Locate every Plasmodium ovale-infected red blood cell.
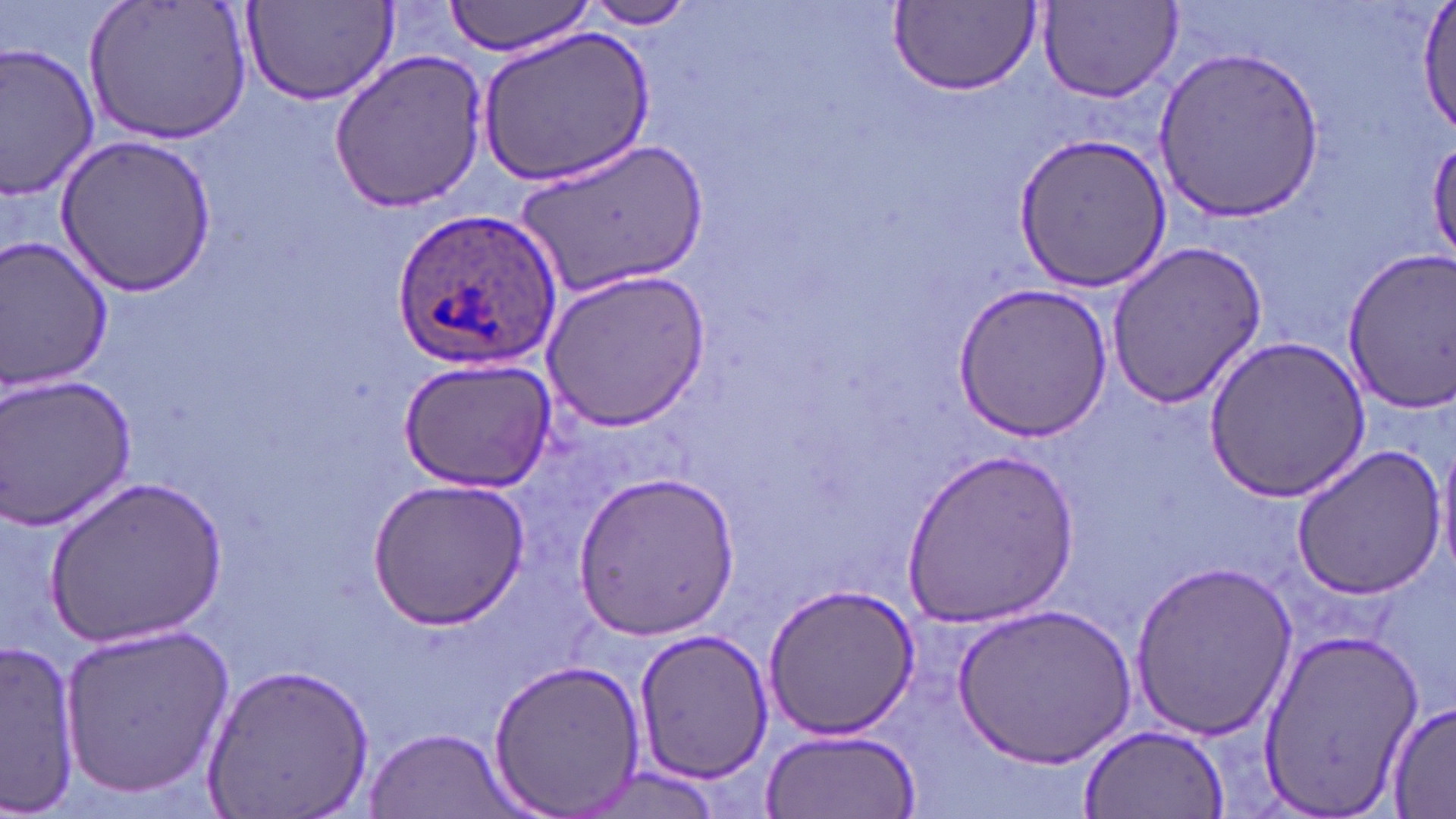
Approximate bounding boxes as named x1/y1/x2/y2 corners in pixels.
Plasmodium ovale-infected red blood cells: (x1=393, y1=206, x2=564, y2=369).

slide_level_diagnosis: Plasmodium ovale
magnification: 1000x
field_of_view: single
image_size: 1456×819 pixels
stain: May-Grünwald-Giemsa
preparation: thin blood smear
uninfected_red_blood_cell_locations: 'approximate bounding boxes as named x1/y1/x2/y2 corners in pixels: (x1=85, y1=0, x2=253, y2=144), (x1=440, y1=0, x2=600, y2=55), (x1=581, y1=0, x2=698, y2=29), (x1=1414, y1=0, x2=1456, y2=137), (x1=890, y1=1, x2=1041, y2=94), (x1=1036, y1=2, x2=1184, y2=104), (x1=242, y1=3, x2=397, y2=107), (x1=479, y1=28, x2=654, y2=185), (x1=0, y1=40, x2=102, y2=201), (x1=1155, y1=44, x2=1323, y2=225), (x1=327, y1=49, x2=492, y2=212), (x1=1012, y1=131, x2=1172, y2=295), (x1=54, y1=135, x2=221, y2=298), (x1=516, y1=136, x2=706, y2=300), (x1=1428, y1=137, x2=1456, y2=269), (x1=0, y1=236, x2=115, y2=396), (x1=1106, y1=239, x2=1269, y2=411), (x1=1340, y1=252, x2=1456, y2=411), (x1=539, y1=268, x2=711, y2=430), (x1=954, y1=283, x2=1112, y2=441), (x1=1204, y1=335, x2=1370, y2=501), (x1=397, y1=356, x2=556, y2=493), (x1=0, y1=373, x2=139, y2=531), (x1=1436, y1=435, x2=1456, y2=582), (x1=1289, y1=444, x2=1448, y2=601), (x1=897, y1=448, x2=1081, y2=626), (x1=575, y1=469, x2=739, y2=637), (x1=47, y1=476, x2=228, y2=646), (x1=368, y1=477, x2=528, y2=626), (x1=1127, y1=559, x2=1297, y2=740), (x1=764, y1=582, x2=920, y2=739), (x1=954, y1=605, x2=1133, y2=769), (x1=58, y1=620, x2=235, y2=800), (x1=1256, y1=626, x2=1421, y2=819), (x1=632, y1=628, x2=772, y2=785), (x1=1, y1=639, x2=81, y2=812), (x1=486, y1=656, x2=647, y2=816), (x1=201, y1=661, x2=374, y2=818), (x1=1385, y1=699, x2=1456, y2=816), (x1=1076, y1=722, x2=1230, y2=818), (x1=760, y1=727, x2=921, y2=816), (x1=364, y1=729, x2=518, y2=818), (x1=573, y1=768, x2=726, y2=817)'
modality: light microscopy